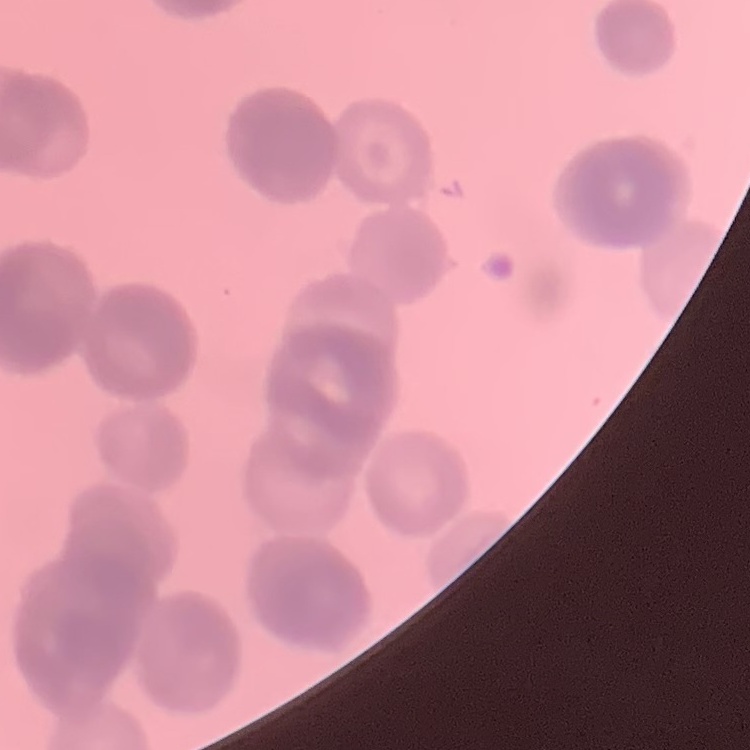

The red blood cells exhibit rouleaux formation. Square crop of a larger photomicrograph. Thin blood smear. Stained with either Field's or Giemsa.